State which parasite is depicted.
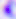
Toxoplasma gondii.

Summary:
  - Modality: micrograph
  - Magnification: 400x